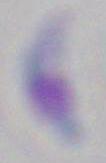
Photomicrograph. Toxoplasma gondii is shown. Captured at 1000x magnification.